Assess the morphology of the erythrocytes.
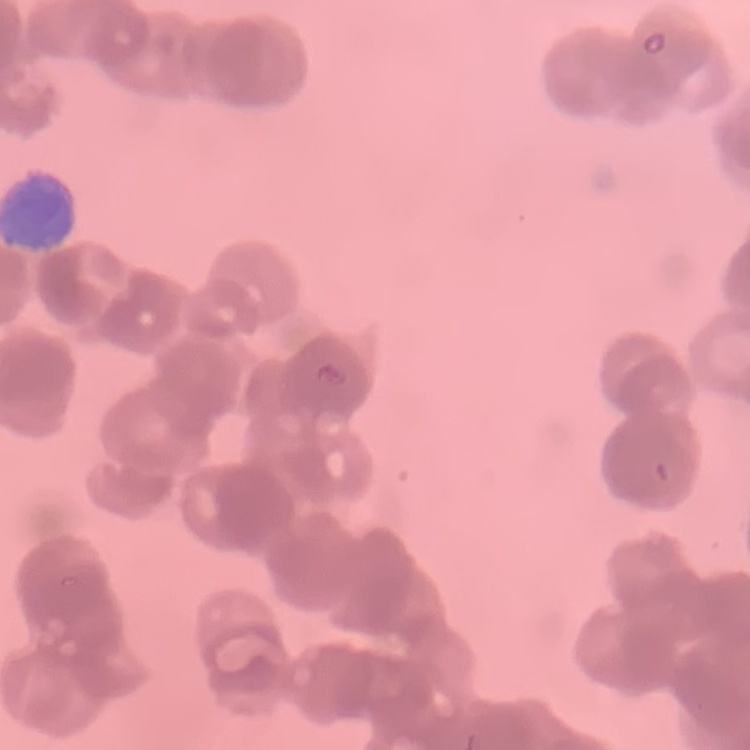
They show rouleaux formation.

stain = Field's or Giemsa
image type = one tile cut from a larger photomicrograph
preparation = thin blood smear